Find each white blood cell.
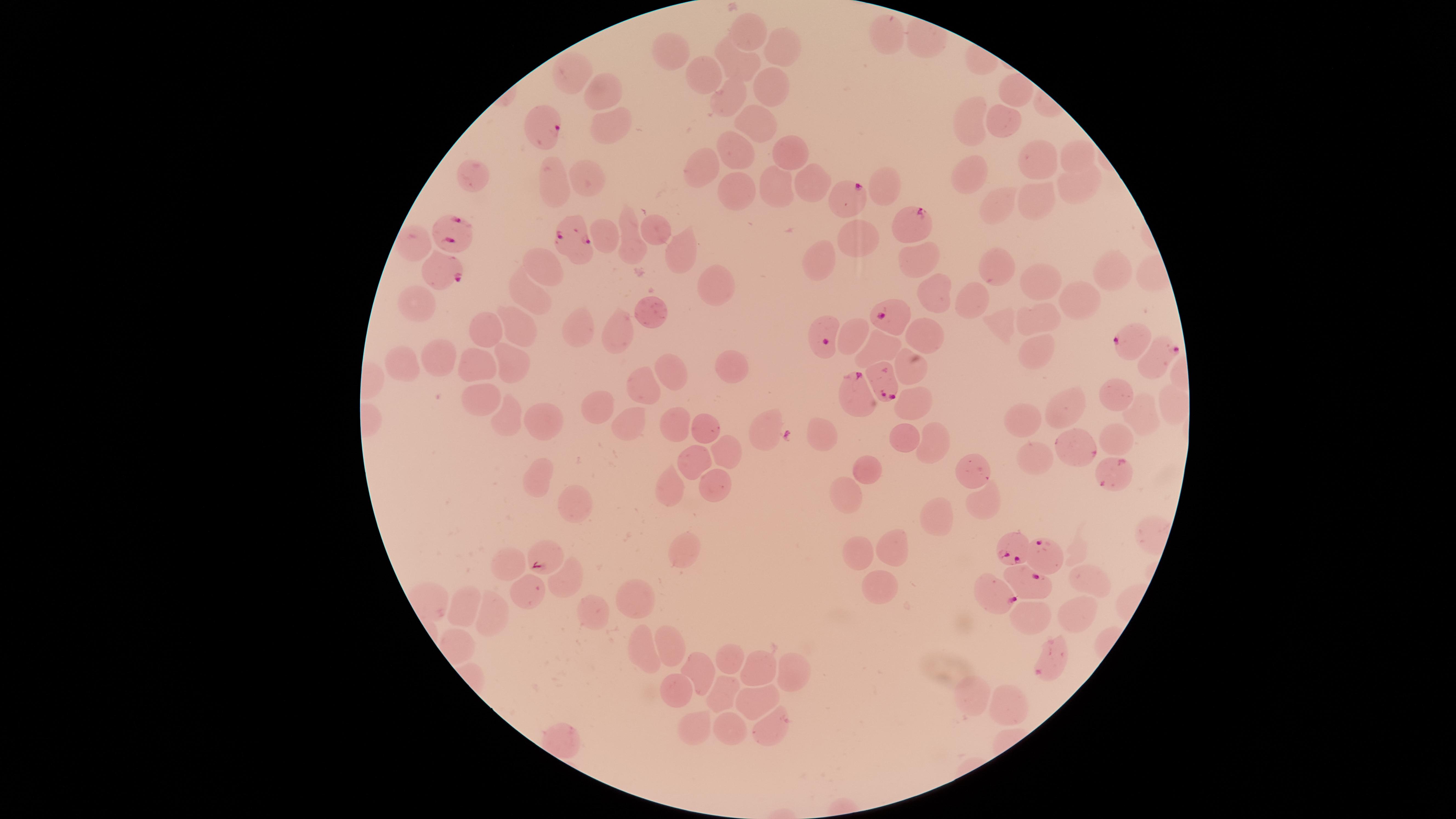

No white blood cells identified.

Approximate marker points as [x, y] in pixels. Uninfected red blood cells: [751, 27], [891, 33], [672, 45], [786, 48], [739, 69], [706, 70], [768, 83], [1014, 86], [605, 90], [724, 96], [969, 118], [1004, 119], [752, 122], [612, 128], [738, 147], [789, 149], [1073, 154], [1028, 156], [965, 166], [703, 167], [472, 174], [588, 174], [808, 180], [550, 181], [1074, 183], [886, 186], [742, 187], [773, 187], [1040, 199], [999, 204], [625, 225], [656, 238], [863, 238], [413, 240], [605, 241], [677, 250], [823, 257], [915, 260], [542, 263], [1000, 269], [1107, 270], [1039, 282], [717, 283], [934, 294], [1085, 294], [531, 295], [977, 299], [417, 302], [656, 313], [1033, 317], [521, 325], [1002, 326], [486, 328], [579, 330], [850, 331], [620, 333], [926, 338], [877, 344], [1033, 348], [406, 360], [435, 361], [916, 361], [732, 363], [473, 366], [508, 366], [673, 366], [646, 388], [1117, 395], [477, 400], [598, 400], [916, 401], [1068, 410], [1141, 413], [506, 415], [542, 420], [670, 421], [768, 421], [1028, 421], [627, 422], [704, 426], [824, 430], [1118, 433], [899, 435], [930, 441], [1073, 448], [731, 450], [1032, 454], [698, 462], [975, 468], [870, 469], [672, 477], [540, 480], [713, 489], [845, 493], [569, 502], [978, 503], [938, 513], [680, 546], [859, 547], [890, 547], [505, 557], [1079, 574], [560, 577], [524, 588], [878, 592], [638, 597], [466, 604], [1074, 608], [488, 613], [593, 613], [1035, 615], [674, 641], [646, 643], [729, 659], [756, 664], [791, 675], [701, 677], [675, 689], [720, 690], [975, 696], [762, 700], [1005, 700], [694, 722], [727, 729], [772, 729]. Parasitized red blood cells: [540, 128], [853, 198], [916, 220], [453, 231], [573, 240], [442, 267], [892, 320], [819, 332], [1135, 338], [1160, 359], [885, 378], [852, 396], [1107, 476], [1005, 543], [1049, 554], [546, 555], [1031, 583], [997, 595]. Giemsa-stained preparation. Presence: malaria parasites detected. Species: Plasmodium falciparum. Smartphone photograph through the microscope eyepiece. The visible region is circular. Thin smear of blood. Single field of view. Image is 1456×819 pixels.